Outline platelets.
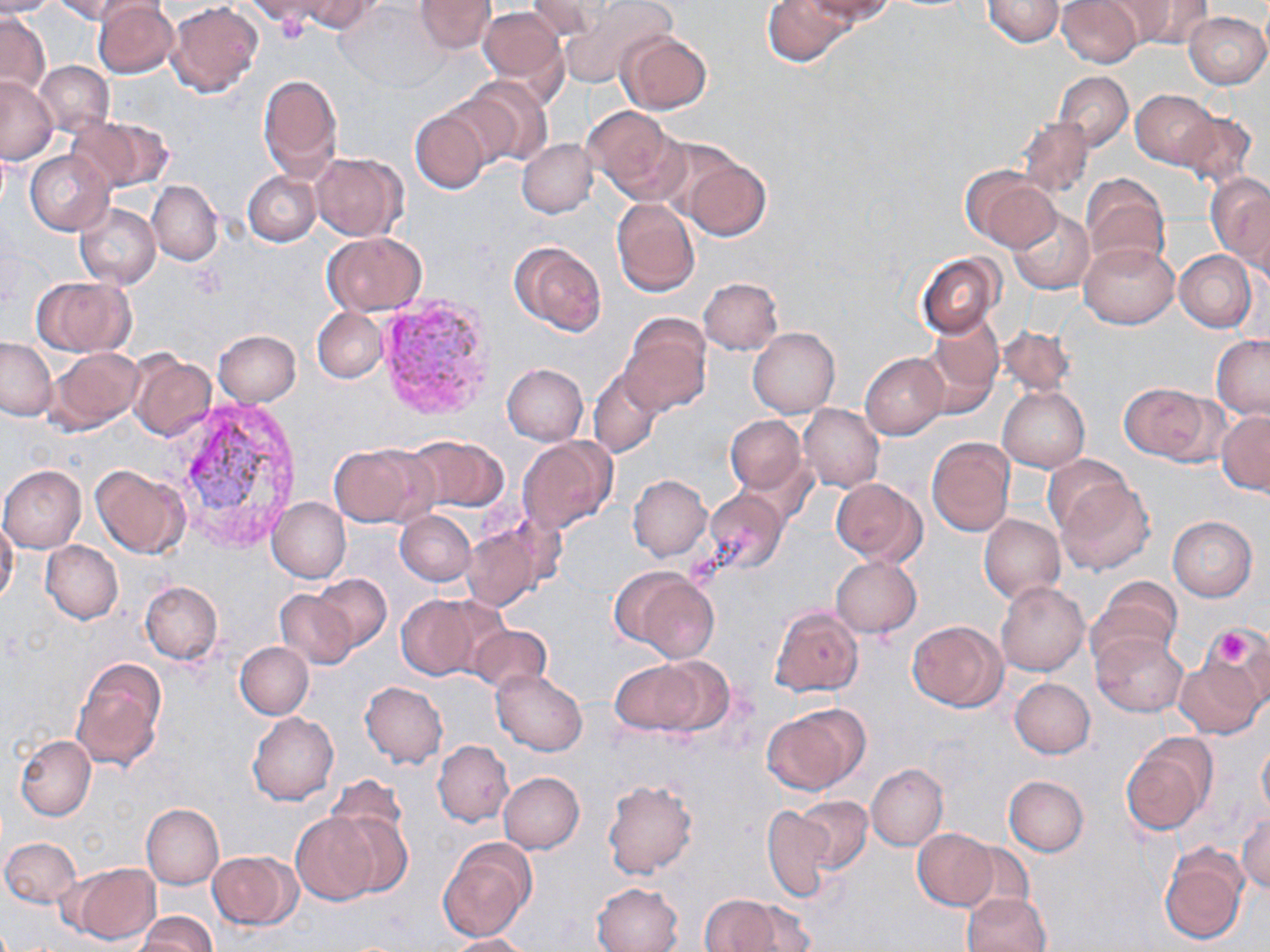
Approximate bounding boxes as (x1, y1, x2, y2) in pixels.
Platelets: (273, 11, 309, 46), (1209, 627, 1259, 668).

Plasmodium vivax-infected red blood cell locations: (374, 293, 496, 421), (171, 391, 305, 548). Uninfected red blood cell locations: (0, 0, 57, 16), (52, 0, 144, 24), (294, 0, 378, 34), (415, 0, 494, 54), (558, 0, 675, 90), (761, 0, 853, 67), (805, 0, 895, 28), (982, 0, 1064, 46), (1055, 0, 1143, 67), (1118, 0, 1213, 48), (93, 1, 178, 78), (526, 1, 614, 45), (167, 2, 263, 97), (337, 2, 443, 93), (479, 6, 567, 90), (0, 12, 51, 100), (1183, 12, 1269, 88), (617, 31, 711, 115), (35, 61, 113, 135), (1054, 71, 1133, 151), (258, 73, 342, 179), (457, 76, 553, 168), (0, 77, 57, 163), (1131, 89, 1219, 170), (581, 106, 682, 201), (410, 109, 491, 194), (1174, 112, 1257, 189), (66, 116, 174, 193), (1016, 118, 1092, 197), (517, 139, 599, 218), (25, 150, 113, 235), (310, 151, 407, 240), (682, 158, 770, 242), (963, 169, 1061, 252), (243, 172, 321, 246), (1205, 173, 1270, 265), (1080, 174, 1169, 271), (147, 180, 222, 265), (611, 199, 700, 297), (75, 203, 161, 288), (1008, 208, 1094, 293), (323, 234, 427, 315), (510, 240, 606, 335), (1079, 241, 1178, 328), (1174, 249, 1256, 332), (916, 253, 1003, 338), (33, 277, 133, 356), (699, 277, 783, 355), (313, 307, 387, 383), (621, 316, 711, 416), (920, 318, 1005, 416), (748, 327, 840, 416), (998, 327, 1074, 398), (213, 330, 300, 407), (1211, 334, 1270, 418), (0, 338, 55, 419), (46, 347, 143, 435), (129, 353, 216, 440), (861, 353, 948, 438), (501, 363, 588, 444), (589, 368, 664, 458), (1118, 381, 1221, 463), (998, 387, 1089, 471), (799, 404, 884, 492), (1216, 411, 1270, 496), (724, 415, 808, 497), (403, 436, 509, 513), (517, 436, 617, 536), (927, 437, 1016, 537), (328, 445, 424, 526), (1043, 454, 1132, 537), (296, 459, 407, 550), (91, 465, 188, 558), (0, 466, 87, 552), (628, 475, 712, 561), (831, 478, 925, 567), (1055, 481, 1155, 575), (703, 488, 789, 575), (267, 496, 350, 583), (394, 510, 476, 586), (979, 513, 1064, 603), (1167, 516, 1257, 601), (0, 517, 19, 606), (460, 524, 547, 612), (41, 541, 123, 624), (831, 557, 922, 638), (613, 565, 719, 661), (310, 573, 392, 650), (1094, 575, 1182, 660), (140, 581, 222, 665), (995, 582, 1090, 676), (274, 589, 362, 671), (395, 593, 501, 681), (770, 605, 863, 696), (907, 620, 1007, 711), (466, 624, 551, 694), (1092, 632, 1187, 718), (1217, 633, 1270, 710), (235, 642, 313, 718), (1174, 656, 1264, 738), (72, 660, 166, 771), (611, 660, 711, 736), (492, 669, 587, 755), (1010, 677, 1095, 758), (360, 682, 448, 768), (763, 704, 868, 794), (248, 712, 339, 805), (16, 735, 95, 821), (1121, 735, 1216, 836), (433, 740, 513, 826), (1257, 740, 1270, 819), (866, 764, 948, 849), (499, 773, 583, 853), (1004, 776, 1088, 856), (602, 778, 697, 877), (328, 797, 414, 894), (797, 797, 873, 872), (140, 803, 224, 889), (763, 806, 832, 902), (291, 812, 378, 906), (1237, 813, 1270, 894), (914, 828, 998, 909), (1, 836, 81, 907), (439, 839, 535, 939), (955, 842, 1034, 917), (1158, 845, 1248, 946), (208, 850, 300, 930), (72, 862, 160, 944), (593, 882, 683, 952), (962, 892, 1051, 952), (701, 893, 805, 951), (139, 912, 216, 952), (445, 934, 530, 952). Slide-level diagnosis: Plasmodium vivax. Single field of view. Light microscopy. Captured at 1000x magnification. Thin blood smear. Image is 1270×952 pixels. May-Grünwald-Giemsa-stained preparation.